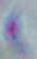

Summary:
  - Magnification: 1000x
  - Modality: micrograph
  - Identification: Toxoplasma gondii